State the preparation type.
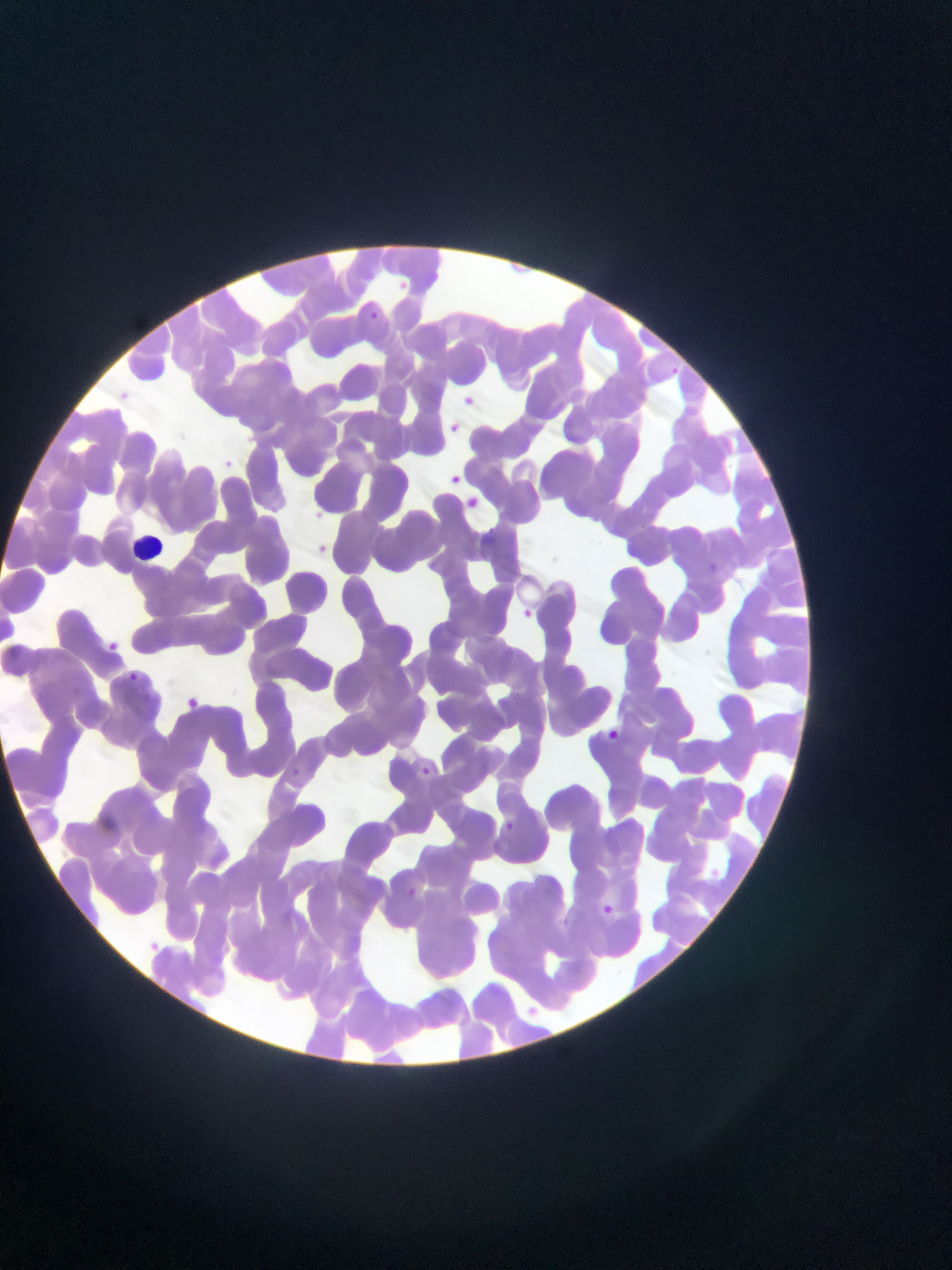
This is a thin smear.

Approximate bounding boxes as (left, top, right, bottom) in pixels. Leukocyte locations: (136, 532, 173, 560). Malaria parasite locations: (397, 276, 411, 297), (366, 307, 380, 323), (671, 362, 681, 376), (120, 388, 131, 400), (462, 389, 472, 403), (446, 413, 462, 432), (222, 456, 241, 474), (451, 465, 471, 484), (461, 493, 485, 512), (312, 502, 331, 519), (316, 537, 330, 554), (522, 602, 536, 619), (107, 636, 127, 652), (129, 672, 138, 680), (183, 695, 206, 714), (607, 725, 625, 743), (419, 764, 440, 781), (504, 816, 518, 830), (103, 817, 116, 830), (408, 884, 425, 898), (600, 901, 623, 921). Mobile-phone photograph taken through the microscope. Image is 952×1270 pixels. One field of view. Collected in Ghana.